Report the malaria status of this cell.
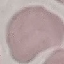

Uninfected.

Summary:
  - Image type: automatically extracted cell patch, resized to 64 × 64 pixels
  - Stain: Giemsa
  - Capture: smartphone camera at the microscope eyepiece
  - Preparation: thin blood film